Name the parasite shown.
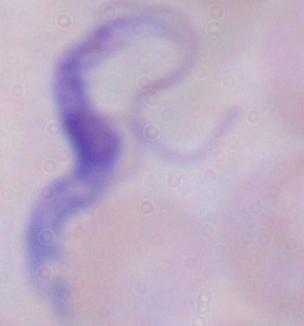
This is a trypanosome.

Summary:
  - Magnification: 1000x
  - Modality: micrograph